Assess this cell for malaria.
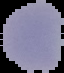

Parasitized.

Image is 64×73 pixels. From a thin blood film. Segmented cell region on a black background.